State which cell type is depicted.
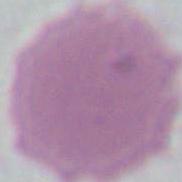

An erythrocyte.

Captured at 1000x magnification. Micrograph.